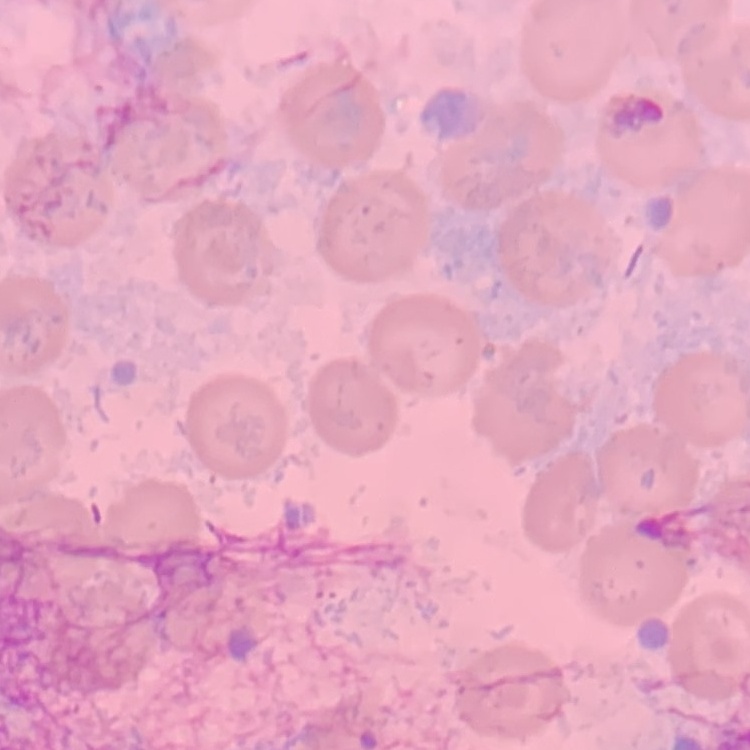 The erythrocytes show no rouleaux formation. Square crop of a larger photomicrograph. Field's or Giemsa stain. Thin peripheral smear.